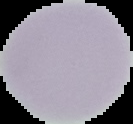
Cell region segmented out of the field of view; the surrounding area is masked to black. Result: no malaria parasites seen. From a thin blood smear. Image is 133×124 pixels.